Assess this cell for malaria.
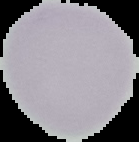
It is uninfected.

image type = segmented cell region on a black background
image size = 139×142 pixels
preparation = thin blood film